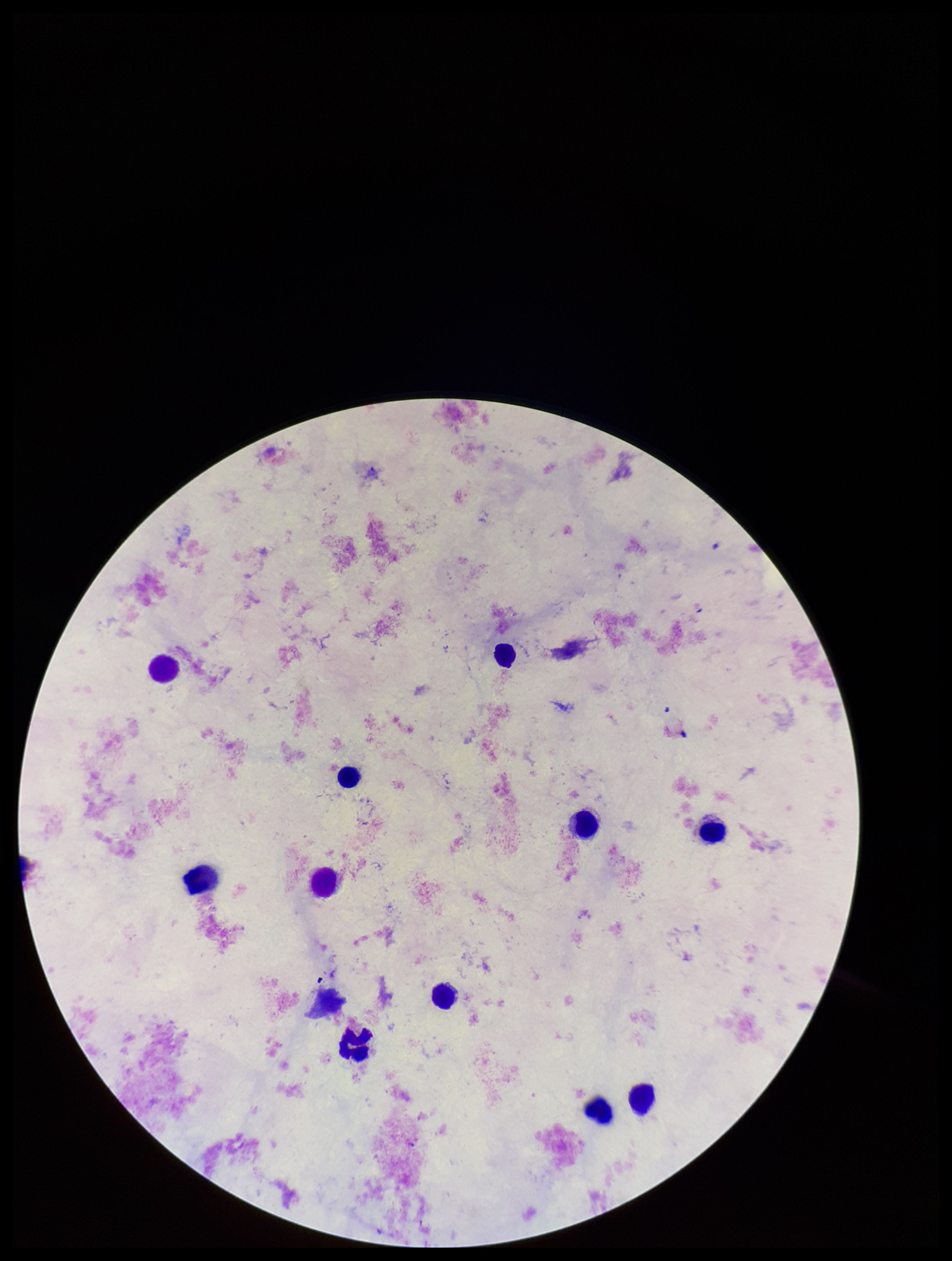
Photographed through the microscope eyepiece with a smartphone camera. Stained with Giemsa. One field from this slide. Parasite count: 0. Plasmodium parasites: none seen. Leukocyte count: 12. Image is 952×1261 pixels. Preparation: thick blood smear. Patient malaria status: negative.